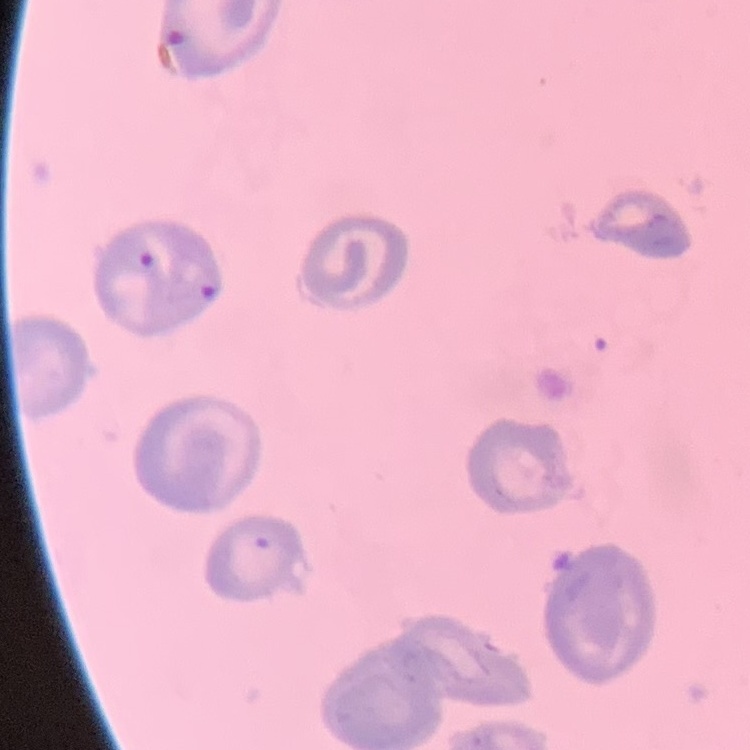
Summary:
  - Erythrocyte morphology: no rouleaux formation
  - Preparation: thin peripheral smear
  - Image type: one tile cut from a larger photomicrograph
  - Stain: Field's or Giemsa